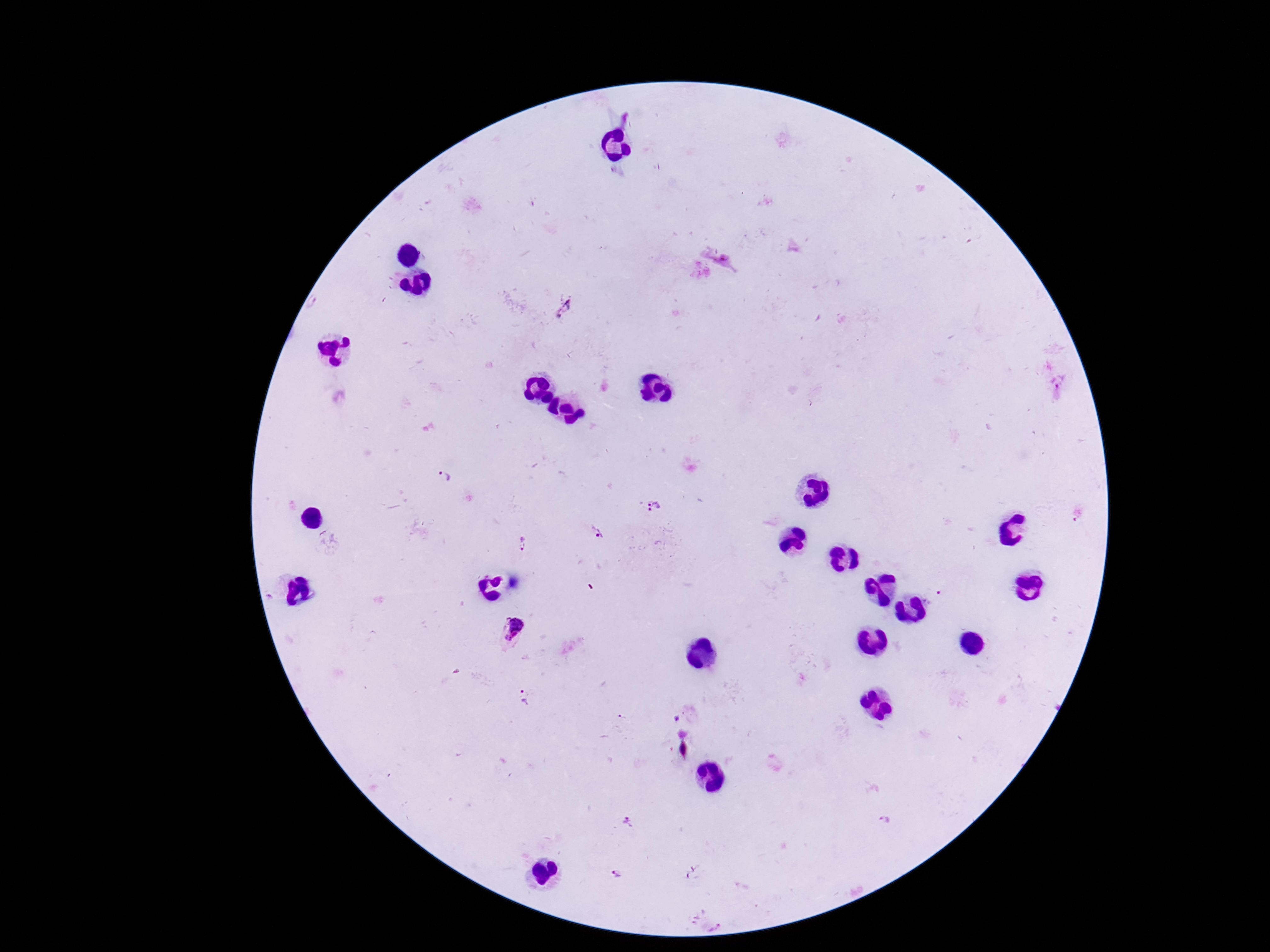
magnification = 100x
stain = Giemsa
Plasmodium parasite locations = approximate centers as [x, y] in pixels: [446, 480], [653, 505], [596, 532], [520, 543], [513, 632], [525, 697], [884, 819], [627, 822], [613, 877]
image size = 1270×952 pixels
preparation = thick peripheral-blood smear
patient malaria status = positive
capture = smartphone camera through the microscope eyepiece
field of view = one from this slide